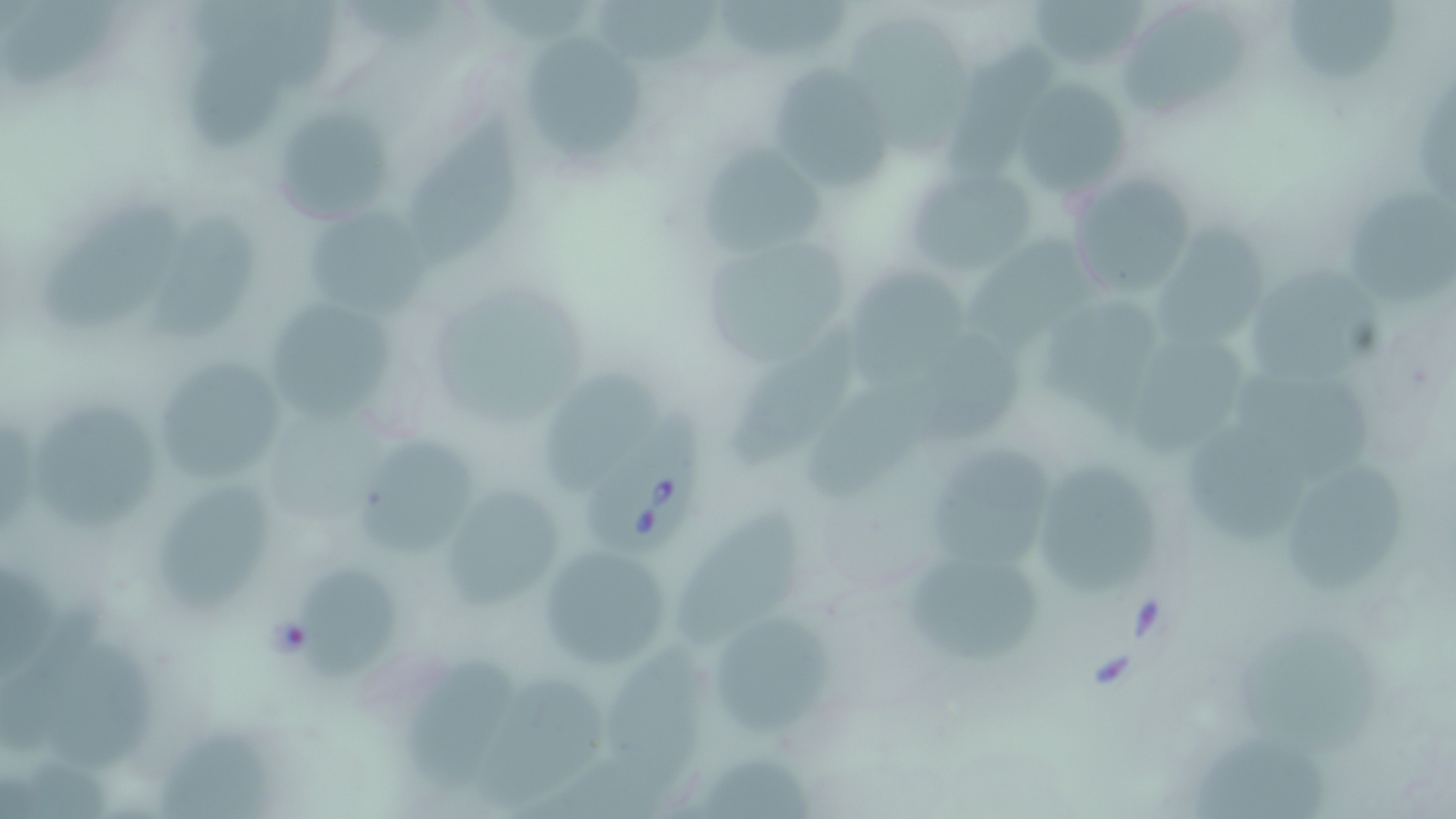
{
  "slide_level_diagnosis": "Babesia divergens",
  "field_of_view": "single",
  "magnification": "1000x",
  "uninfected_red_blood_cell_locations": "approximate bounding boxes as (x1, y1, x2, y2) in pixels: (598, 0, 720, 70), (719, 0, 851, 54), (1024, 0, 1148, 66), (1282, 0, 1399, 82), (1119, 6, 1255, 121), (847, 18, 979, 160), (527, 34, 641, 164), (780, 61, 886, 194), (1013, 77, 1129, 195), (266, 103, 402, 226), (405, 107, 530, 266), (703, 150, 829, 255), (906, 166, 1037, 276), (1067, 171, 1201, 299), (1347, 186, 1456, 308), (38, 197, 186, 332), (304, 213, 430, 318), (154, 217, 259, 340), (1159, 217, 1275, 347), (966, 220, 1111, 358), (689, 226, 856, 368), (843, 260, 968, 391), (1251, 267, 1386, 385), (425, 284, 591, 419), (269, 301, 402, 422), (1045, 304, 1167, 430), (726, 318, 863, 466), (1129, 337, 1250, 461), (136, 352, 296, 488), (1231, 362, 1380, 477), (542, 374, 662, 489), (37, 408, 157, 531), (1187, 421, 1309, 544), (356, 435, 482, 556), (933, 441, 1049, 567), (1039, 457, 1161, 596), (1286, 458, 1411, 590), (157, 474, 276, 614), (437, 484, 570, 613), (677, 500, 813, 652), (536, 542, 675, 670), (901, 545, 1046, 664), (295, 574, 403, 685), (717, 619, 840, 736), (1240, 621, 1386, 764), (41, 628, 159, 777), (602, 644, 708, 799), (407, 649, 517, 793), (473, 663, 615, 801), (157, 731, 270, 817), (1192, 731, 1331, 819), (701, 749, 817, 819)",
  "preparation": "thin blood smear",
  "image_size": "1456×819 pixels",
  "stain": "May-Grünwald-Giemsa",
  "modality": "light microscopy",
  "babesia_divergens_infected_red_blood_cell_locations": "approximate bounding boxes as (x1, y1, x2, y2) in pixels: (579, 404, 713, 553)"
}